Report the malaria status of this cell.
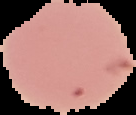
Uninfected.

preparation = thin blood film
image size = 136×115 pixels
image type = cell region segmented out of the field of view; surrounding area masked to black